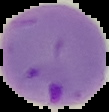

malaria status = parasitized
image type = segmented cell region on a black background
image size = 109×112 pixels
preparation = thin blood film